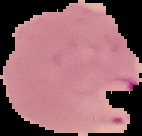
result = malaria parasites detected
image size = 142×136 pixels
preparation = thin blood film
image type = segmented cell region with the area outside set to black